Classify this cell by malaria status.
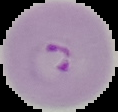

It is parasitized.

Image is 118×112 pixels. From a thin blood film. Segmented cell region on a black background.